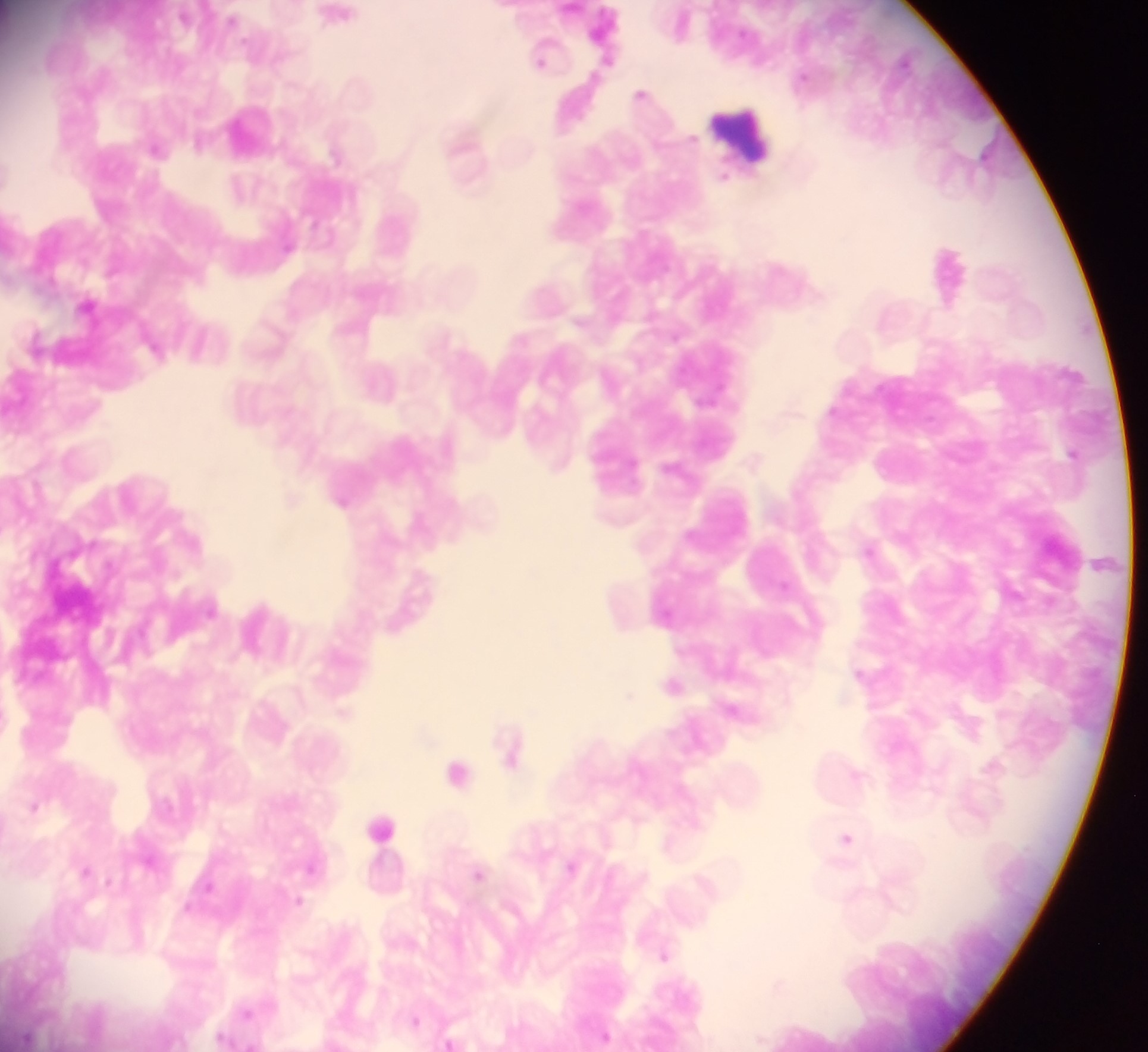
country = Ghana
leukocyte locations = approximate centers as x y in pixels: 740 144; 381 825
preparation = thick blood smear
Plasmodium parasite locations = approximate centers as x y in pixels: 339 14; 542 53; 641 93; 155 348; 870 549; 785 584; 859 673; 673 684; 629 695; 734 709; 511 749; 458 771; 857 774; 35 805; 846 837; 571 866; 311 867; 85 870; 478 873; 298 901; 665 954; 778 984; 246 1011; 415 1019; 605 1036; 449 1041
field of view = single
capture = mobile-phone photograph through a microscope
image size = 1148×1052 pixels